Report the malaria status of this cell.
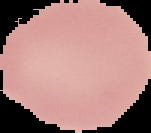

It is uninfected.

{
  "image_size": "151×133 pixels",
  "image_type": "segmented cell region with the area outside set to black",
  "preparation": "thin blood film"
}